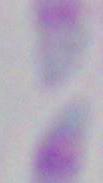

Captured at 1000x magnification. Photomicrograph. Toxoplasma gondii is shown.